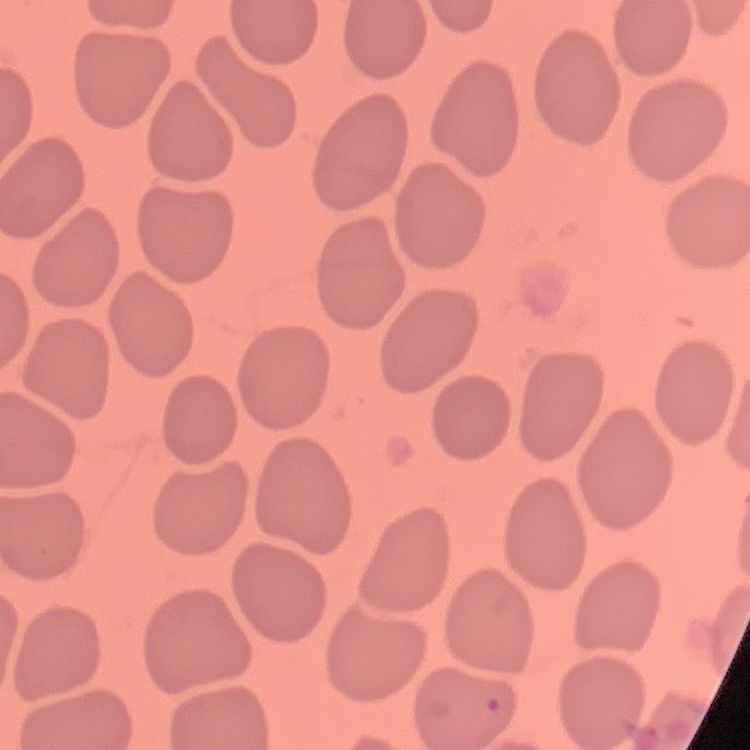
The erythrocytes show no rouleaux formation. Thin blood film. Square crop of a larger photomicrograph. Field's or Giemsa stain.